Assess the morphology of the red blood cells.
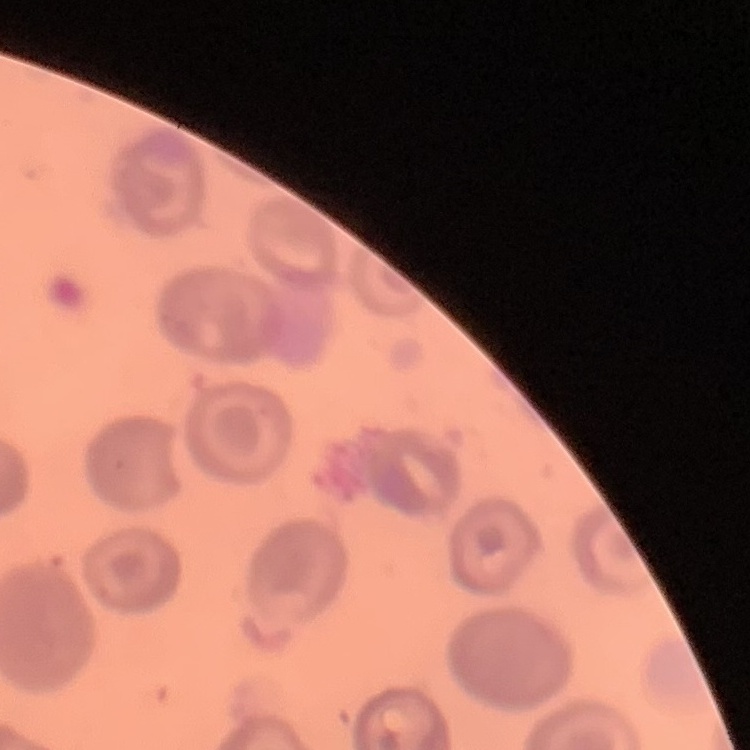
No rouleaux formation.

Square crop of a larger photomicrograph. Thin blood film. Stained with either Field's or Giemsa.